Assess this cell for malaria.
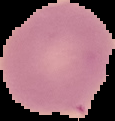
It is uninfected.

From a thin blood smear. The area outside the segmented cell region is set to black. Image is 115×121 pixels.